Name the parasite shown.
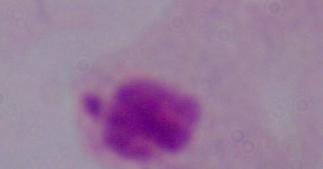
A trichomonad.

Summary:
  - Magnification: 1000x
  - Modality: micrograph